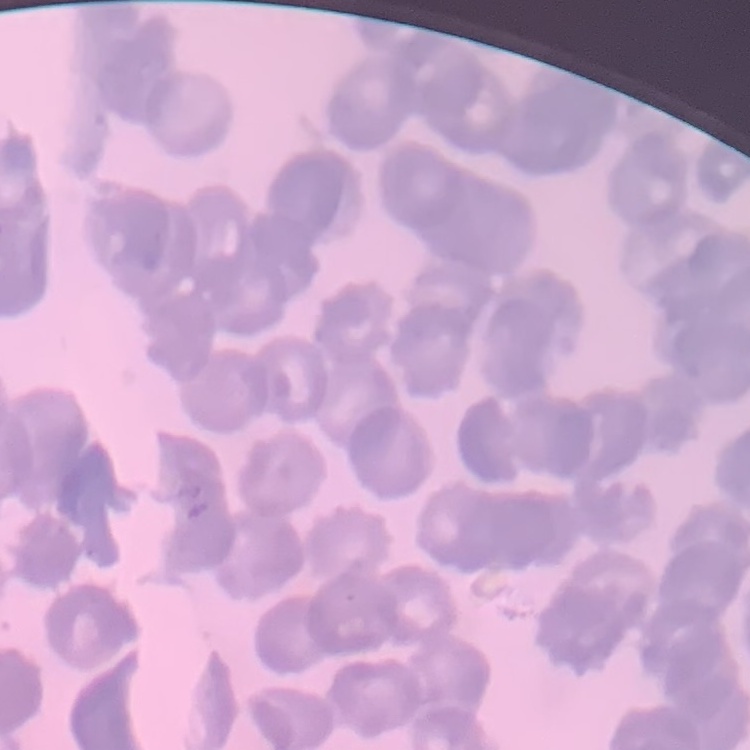 The red blood cells show rouleaux formation. Thin blood smear. Square crop of a larger photomicrograph. Field's or Giemsa stain.